Identify the cell.
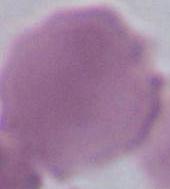
An erythrocyte.

Captured at 1000x magnification. Photomicrograph.